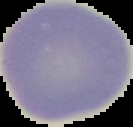

Cell region segmented out of the field of view; the surrounding area is masked to black. Malaria status: uninfected. From a thin blood smear. Image is 133×127 pixels.